Locate every blood parasite and identify its species.
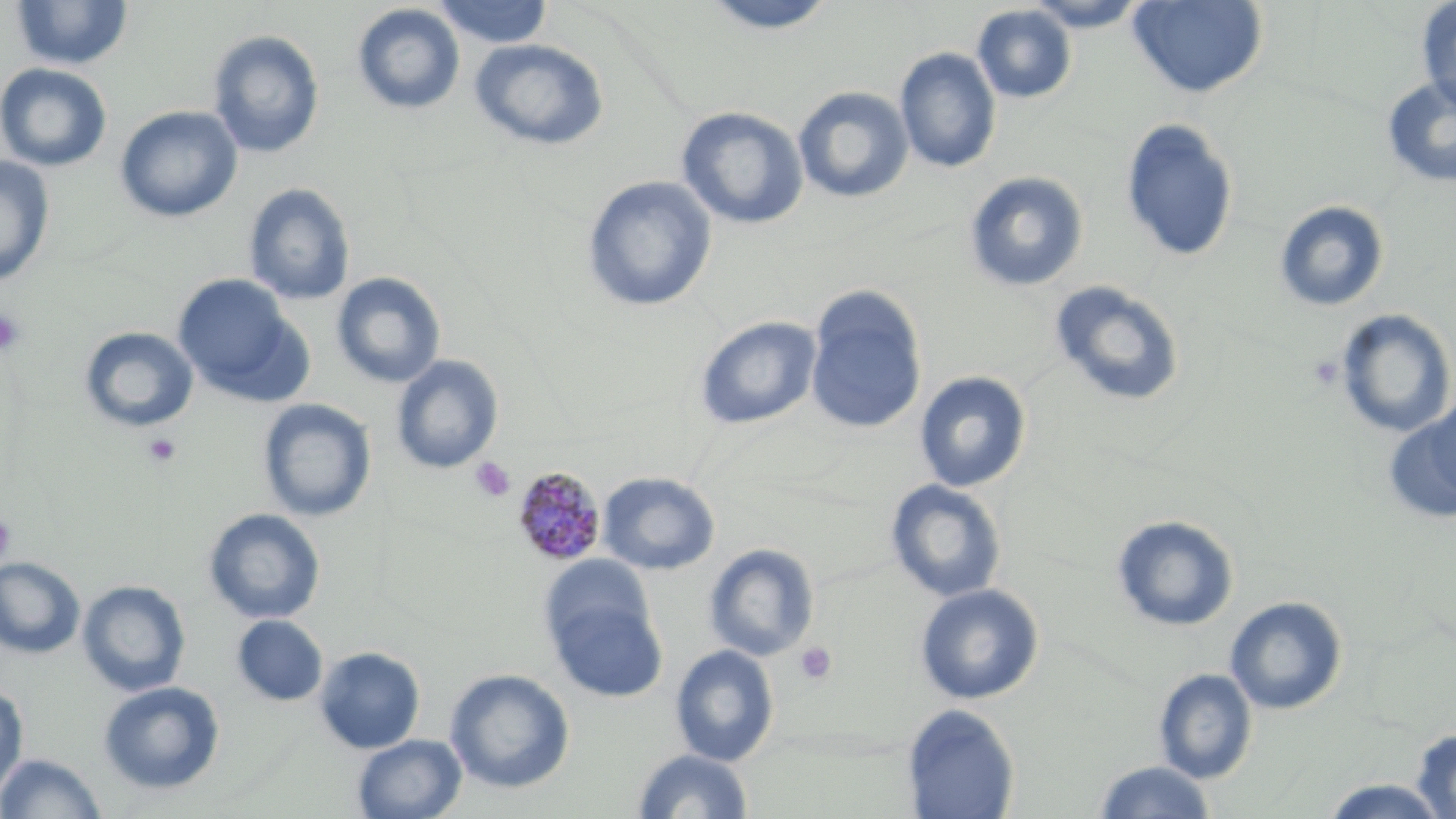

Approximate bounding boxes as named x1/y1/x2/y2 corners in pixels.
Plasmodium malariae-infected red blood cells: (x1=510, y1=466, x2=606, y2=566).
No Plasmodium falciparum, Plasmodium ovale, Plasmodium vivax, Babesia divergens, or Trypanosoma brucei observed.

slide-level diagnosis = Plasmodium malariae
stain = May-Grünwald-Giemsa
uninfected red blood cell locations = approximate bounding boxes as named x1/y1/x2/y2 corners in pixels: (x1=433, y1=0, x2=552, y2=48), (x1=699, y1=0, x2=840, y2=34), (x1=1023, y1=0, x2=1151, y2=31), (x1=1416, y1=0, x2=1456, y2=114), (x1=11, y1=1, x2=133, y2=70), (x1=1128, y1=1, x2=1267, y2=98), (x1=352, y1=4, x2=465, y2=115), (x1=972, y1=4, x2=1077, y2=104), (x1=207, y1=29, x2=325, y2=158), (x1=470, y1=39, x2=609, y2=151), (x1=895, y1=47, x2=1002, y2=174), (x1=0, y1=62, x2=112, y2=171), (x1=1382, y1=75, x2=1456, y2=189), (x1=793, y1=85, x2=914, y2=204), (x1=115, y1=105, x2=243, y2=223), (x1=675, y1=106, x2=809, y2=230), (x1=1120, y1=117, x2=1240, y2=262), (x1=0, y1=156, x2=55, y2=287), (x1=964, y1=171, x2=1089, y2=291), (x1=582, y1=175, x2=717, y2=312), (x1=243, y1=183, x2=356, y2=305), (x1=1274, y1=200, x2=1390, y2=312), (x1=331, y1=272, x2=446, y2=388), (x1=172, y1=273, x2=307, y2=404), (x1=1049, y1=280, x2=1186, y2=407), (x1=805, y1=287, x2=927, y2=436), (x1=1333, y1=308, x2=1455, y2=438), (x1=695, y1=315, x2=822, y2=430), (x1=79, y1=327, x2=199, y2=432), (x1=391, y1=355, x2=504, y2=474), (x1=914, y1=371, x2=1031, y2=492), (x1=1384, y1=398, x2=1456, y2=523), (x1=257, y1=399, x2=377, y2=522), (x1=598, y1=471, x2=720, y2=575), (x1=885, y1=479, x2=1007, y2=602), (x1=203, y1=508, x2=326, y2=624), (x1=1111, y1=514, x2=1239, y2=632), (x1=703, y1=543, x2=820, y2=661), (x1=539, y1=554, x2=656, y2=663), (x1=0, y1=557, x2=85, y2=658), (x1=77, y1=579, x2=191, y2=696), (x1=915, y1=584, x2=1044, y2=704), (x1=547, y1=593, x2=667, y2=702), (x1=1225, y1=596, x2=1347, y2=715), (x1=232, y1=615, x2=328, y2=706), (x1=670, y1=644, x2=780, y2=766), (x1=314, y1=646, x2=425, y2=753), (x1=445, y1=668, x2=575, y2=794), (x1=1153, y1=668, x2=1258, y2=784), (x1=98, y1=681, x2=225, y2=795), (x1=0, y1=684, x2=28, y2=797), (x1=901, y1=703, x2=1020, y2=819), (x1=1410, y1=727, x2=1456, y2=819), (x1=352, y1=734, x2=467, y2=818), (x1=632, y1=748, x2=754, y2=818), (x1=0, y1=752, x2=106, y2=819), (x1=1093, y1=760, x2=1216, y2=818), (x1=1317, y1=777, x2=1451, y2=818)
image size = 1456×819 pixels
magnification = 1000x
field of view = single
platelet locations = approximate bounding boxes as named x1/y1/x2/y2 corners in pixels: (x1=0, y1=308, x2=26, y2=356), (x1=142, y1=433, x2=182, y2=467), (x1=470, y1=457, x2=515, y2=502), (x1=0, y1=513, x2=17, y2=566), (x1=795, y1=642, x2=837, y2=686)
modality = optical microscopy
preparation = thin blood smear